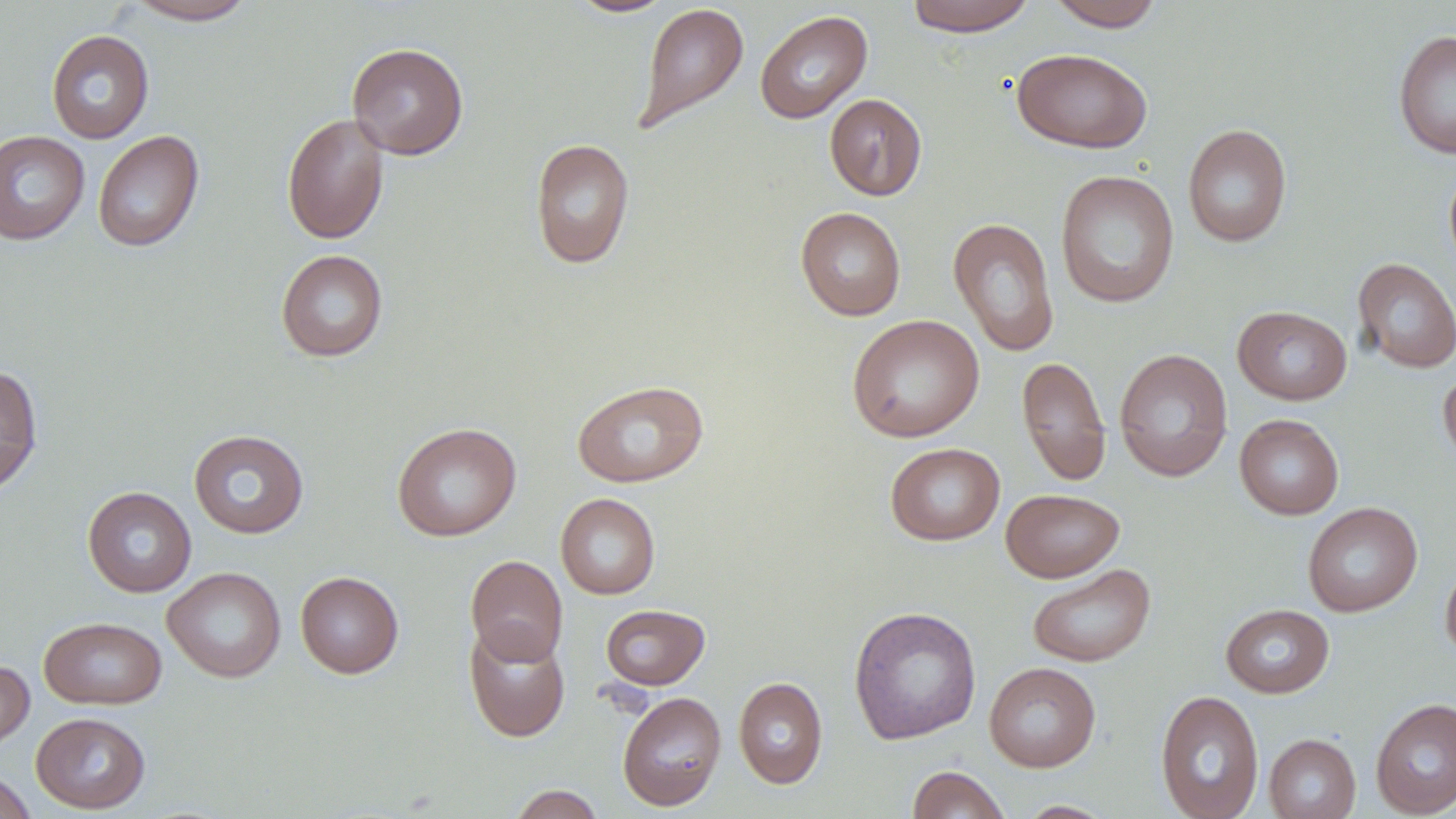

Summary:
  - Coordinate format: approximate bounding boxes as named x1/y1/x2/y2 corners in pixels
  - Uninfected red blood cell locations: (x1=124, y1=0, x2=257, y2=24), (x1=905, y1=0, x2=1036, y2=36), (x1=566, y1=1, x2=677, y2=18), (x1=1046, y1=1, x2=1165, y2=32), (x1=633, y1=2, x2=749, y2=134), (x1=754, y1=10, x2=873, y2=124), (x1=46, y1=29, x2=155, y2=144), (x1=1393, y1=30, x2=1456, y2=158), (x1=346, y1=42, x2=469, y2=159), (x1=1013, y1=48, x2=1153, y2=153), (x1=824, y1=94, x2=927, y2=201), (x1=281, y1=112, x2=390, y2=245), (x1=1183, y1=123, x2=1292, y2=247), (x1=0, y1=130, x2=90, y2=245), (x1=93, y1=130, x2=204, y2=252), (x1=530, y1=138, x2=635, y2=269), (x1=1054, y1=169, x2=1180, y2=308), (x1=795, y1=206, x2=906, y2=321), (x1=948, y1=217, x2=1060, y2=357), (x1=275, y1=249, x2=388, y2=362), (x1=1352, y1=258, x2=1456, y2=373), (x1=1232, y1=305, x2=1352, y2=404), (x1=847, y1=314, x2=985, y2=443), (x1=1114, y1=348, x2=1233, y2=482), (x1=1017, y1=356, x2=1111, y2=485), (x1=0, y1=364, x2=43, y2=496), (x1=1438, y1=366, x2=1456, y2=471), (x1=572, y1=379, x2=709, y2=487), (x1=1234, y1=414, x2=1344, y2=520), (x1=392, y1=422, x2=521, y2=541), (x1=188, y1=429, x2=309, y2=539), (x1=885, y1=443, x2=1005, y2=545), (x1=82, y1=486, x2=197, y2=598), (x1=1001, y1=488, x2=1125, y2=583), (x1=556, y1=493, x2=660, y2=600), (x1=1302, y1=502, x2=1422, y2=617), (x1=465, y1=555, x2=568, y2=665), (x1=1440, y1=558, x2=1456, y2=662), (x1=1027, y1=563, x2=1156, y2=668), (x1=162, y1=566, x2=286, y2=683), (x1=295, y1=570, x2=404, y2=678), (x1=600, y1=603, x2=710, y2=690), (x1=1220, y1=604, x2=1335, y2=698), (x1=848, y1=605, x2=982, y2=745), (x1=38, y1=616, x2=167, y2=709), (x1=464, y1=623, x2=570, y2=742), (x1=0, y1=659, x2=35, y2=753), (x1=984, y1=662, x2=1101, y2=772), (x1=733, y1=676, x2=828, y2=789), (x1=617, y1=690, x2=727, y2=811), (x1=1154, y1=690, x2=1265, y2=819), (x1=1370, y1=697, x2=1456, y2=818), (x1=30, y1=711, x2=151, y2=813), (x1=1263, y1=733, x2=1361, y2=819), (x1=907, y1=765, x2=1012, y2=819), (x1=0, y1=768, x2=37, y2=819), (x1=508, y1=784, x2=605, y2=819), (x1=1016, y1=800, x2=1116, y2=818)
  - Slide-level diagnosis: no evidence of blood parasites
  - Field of view: one of a larger specimen
  - Magnification: 1000x
  - Preparation: thin blood film
  - Stain: May-Grünwald-Giemsa
  - Modality: optical microscopy
  - Image size: 1456×819 pixels